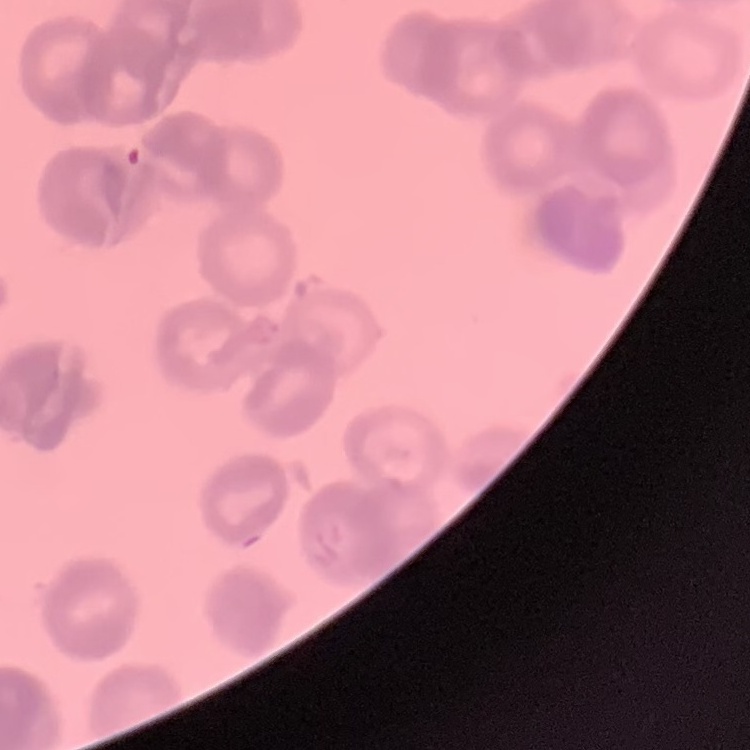
red blood cell morphology = rouleaux formation
stain = Field's or Giemsa
preparation = thin blood film
image type = square crop of a larger photomicrograph